Identify the parasite.
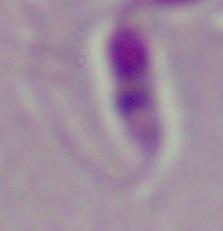
This is Leishmania.

Micrograph. 1000x magnification.